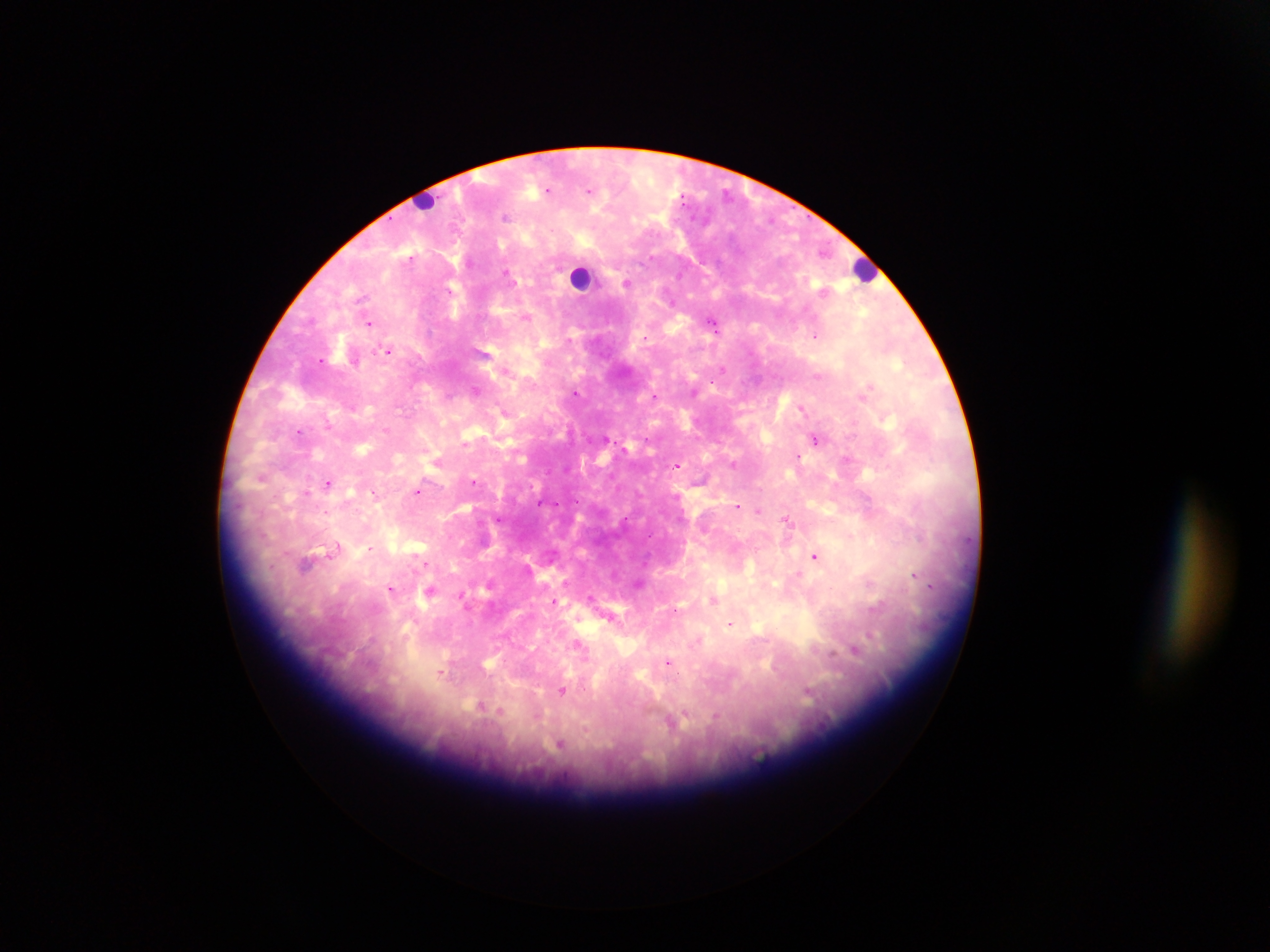 Approximate centers as {x, y} in pixels. Malaria parasite locations: {548, 190}, {589, 191}, {506, 216}, {650, 258}, {508, 273}, {627, 283}, {450, 290}, {362, 299}, {526, 318}, {368, 323}, {713, 324}, {816, 335}, {646, 337}, {569, 340}, {388, 349}, {320, 359}, {722, 369}, {817, 375}, {869, 386}, {475, 390}, {575, 392}, {655, 395}, {863, 395}, {449, 396}, {801, 408}, {503, 411}, {328, 424}, {386, 430}, {300, 431}, {816, 439}, {464, 443}, {798, 457}, {847, 459}, {676, 465}, {733, 465}, {261, 477}, {474, 482}, {327, 483}, {418, 492}, {306, 493}, {374, 493}, {540, 504}, {737, 506}, {759, 510}, {498, 519}, {625, 520}, {787, 520}, {649, 536}, {336, 548}, {371, 548}, {815, 556}, {427, 564}, {306, 565}, {798, 574}, {914, 575}, {638, 583}, {931, 585}, {390, 589}, {430, 592}, {461, 596}, {590, 597}, {714, 600}, {555, 602}, {730, 624}, {580, 646}, {855, 650}, {668, 663}, {443, 673}, {562, 691}, {485, 707}, {674, 722}, {560, 744}. Leukocyte locations: {426, 199}, {863, 270}, {581, 276}. Mobile-phone photograph taken through the microscope. Thick blood film. One field of view. Image is 1270×952 pixels. Sample from Ghana.